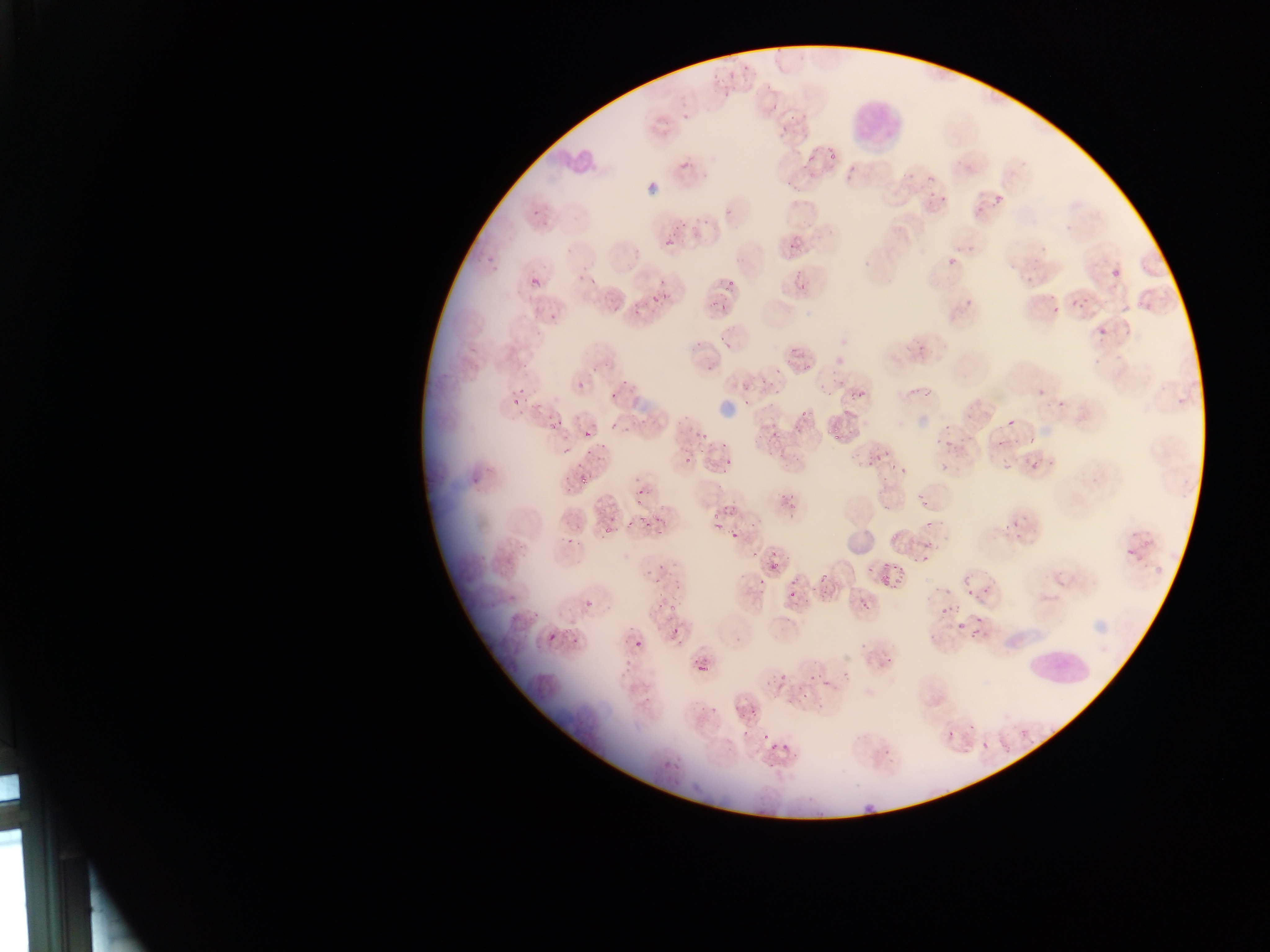

country = Ghana
image size = 1270×952 pixels
field of view = single
Plasmodium parasite locations = approximate bounding boxes as {left, top, right, bottom} in pixels: {723, 52, 753, 76}, {714, 84, 733, 101}, {676, 106, 694, 123}, {775, 111, 802, 137}, {816, 145, 840, 159}, {676, 155, 695, 171}, {918, 171, 945, 200}, {992, 193, 1006, 208}, {539, 212, 562, 231}, {656, 226, 676, 248}, {785, 236, 804, 252}, {481, 243, 503, 272}, {940, 247, 962, 265}, {715, 262, 737, 300}, {572, 263, 596, 290}, {1106, 264, 1127, 287}, {785, 267, 807, 296}, {530, 275, 542, 288}, {649, 275, 671, 291}, {1066, 288, 1088, 309}, {709, 291, 728, 306}, {958, 294, 976, 313}, {649, 298, 659, 306}, {628, 300, 643, 319}, {544, 308, 561, 327}, {1091, 319, 1115, 345}, {909, 334, 928, 358}, {786, 337, 818, 374}, {571, 369, 590, 389}, {753, 371, 775, 399}, {849, 382, 876, 401}, {1033, 384, 1051, 403}, {511, 388, 525, 411}, {609, 390, 620, 401}, {834, 411, 854, 437}, {793, 413, 810, 431}, {1004, 414, 1020, 431}, {547, 415, 565, 433}, {691, 416, 716, 448}, {759, 424, 778, 446}, {584, 430, 598, 441}, {944, 434, 962, 459}, {992, 439, 1001, 451}, {560, 444, 574, 458}, {582, 447, 594, 460}, {675, 448, 694, 467}, {864, 448, 886, 472}, {1028, 453, 1045, 475}, {717, 457, 740, 469}, {999, 459, 1016, 473}, {895, 461, 909, 475}, {559, 466, 573, 486}, {467, 469, 484, 487}, {629, 477, 647, 501}, {580, 479, 592, 487}, {913, 480, 933, 503}, {782, 497, 794, 513}, {703, 501, 726, 531}, {1004, 507, 1028, 540}, {644, 509, 660, 529}, {602, 516, 624, 538}, {731, 531, 740, 541}, {917, 533, 940, 562}, {1121, 538, 1146, 567}, {657, 551, 672, 575}, {768, 559, 780, 572}, {876, 563, 904, 587}, {963, 563, 991, 593}, {786, 576, 808, 601}, {814, 577, 836, 598}, {942, 589, 965, 617}, {577, 591, 601, 613}, {650, 597, 669, 611}, {842, 597, 866, 613}, {952, 614, 976, 638}, {670, 627, 682, 640}, {547, 631, 559, 644}, {634, 639, 646, 650}, {878, 655, 898, 669}, {614, 657, 631, 679}, {696, 659, 710, 674}, {767, 660, 789, 689}, {803, 663, 819, 682}, {819, 665, 838, 692}, {802, 686, 813, 695}, {736, 696, 760, 722}, {942, 726, 963, 749}, {749, 729, 765, 747}, {769, 746, 782, 763}, {658, 749, 674, 773}
preparation = thin blood smear
leukocyte locations = approximate bounding boxes as {left, top, right, bottom} in pixels: {849, 89, 907, 152}, {547, 132, 610, 180}, {1020, 639, 1095, 691}
capture = mobile-phone photograph through a microscope